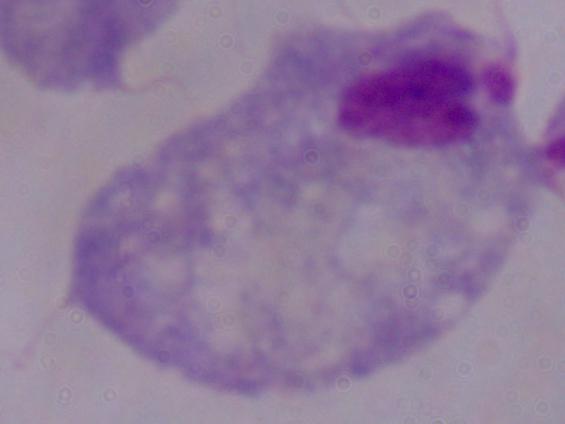
Summary:
  - Magnification: 1000x
  - Identification: trichomonad
  - Modality: photomicrograph